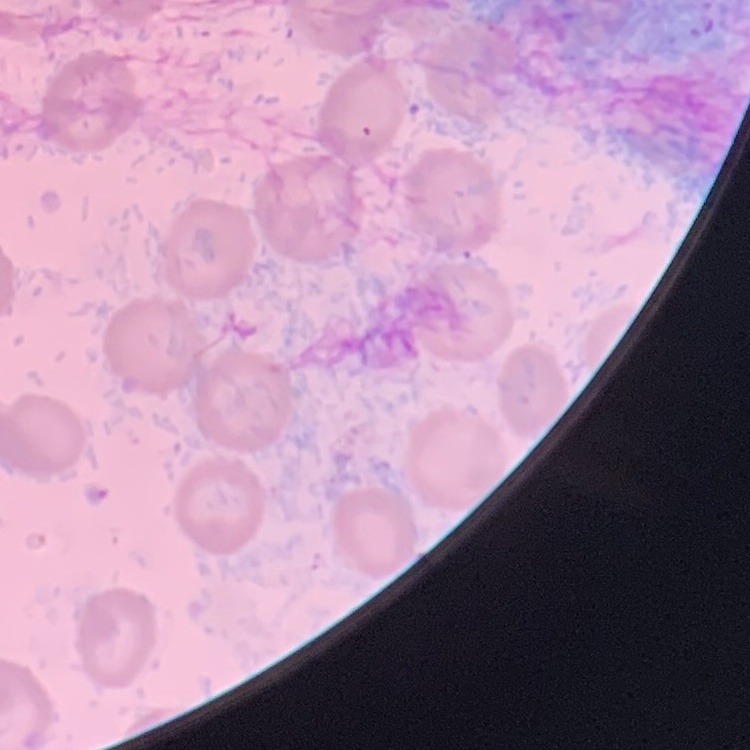 The red blood cells exhibit no rouleaux formation. Thin peripheral smear. One tile cut from a larger photomicrograph. Stained with either Field's or Giemsa.